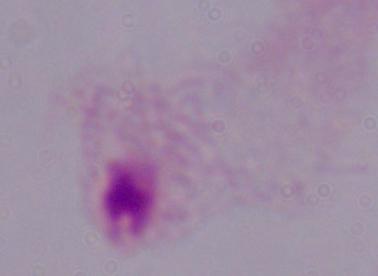
Summary:
  - Modality: photomicrograph
  - Magnification: 1000x
  - Identification: trichomonad